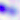
magnification: 400x
modality: photomicrograph
identification: Toxoplasma gondii